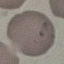
malaria status = uninfected
image type = automatically extracted cell patch, resized to 64 × 64 pixels
preparation = thin blood smear
stain = Giemsa
capture = smartphone through the microscope eyepiece